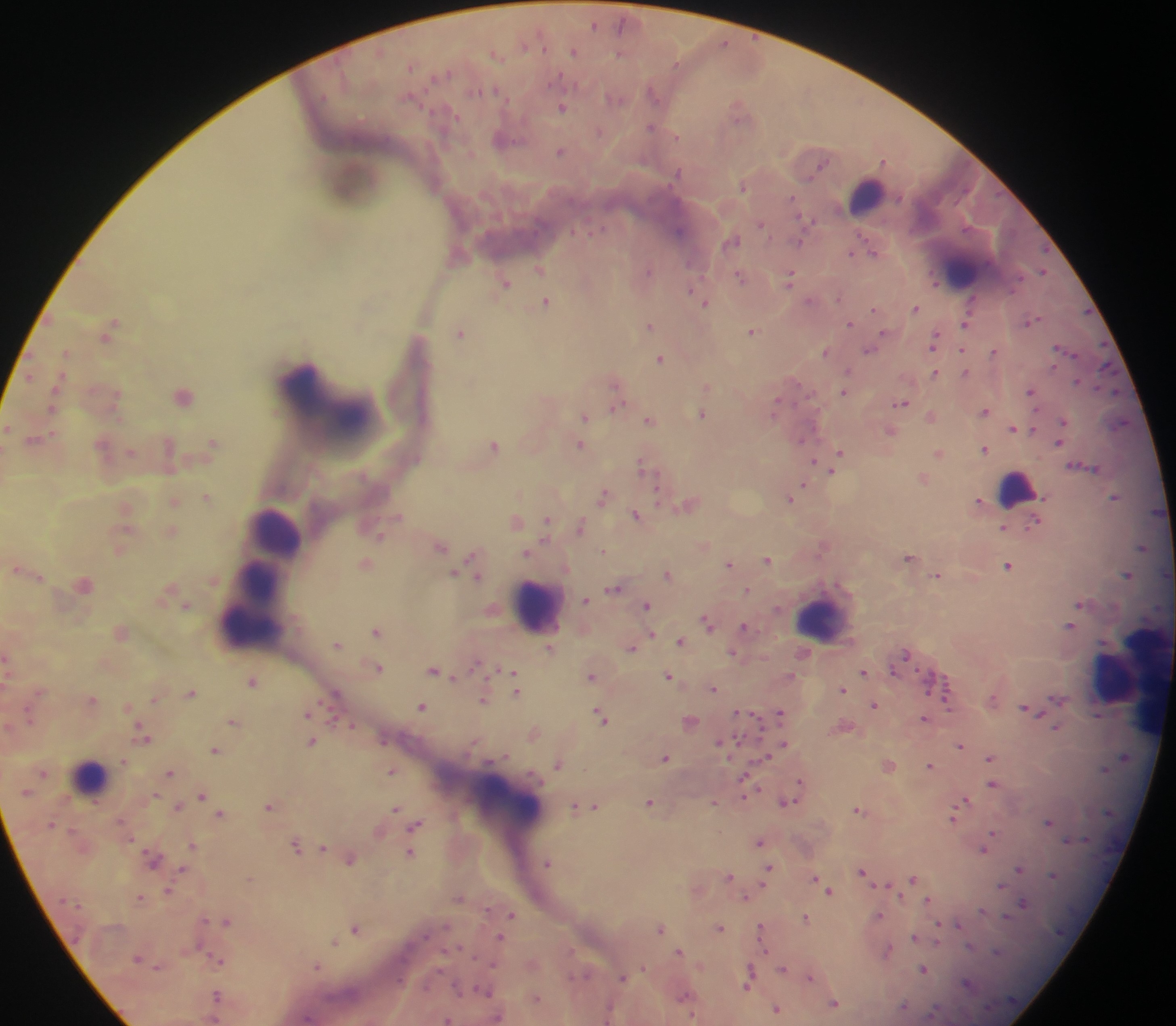
Approximate centers as {x, y} in pixels. Leukocyte locations: {867, 193}, {960, 269}, {1017, 486}, {274, 533}, {262, 592}, {536, 604}, {250, 610}, {823, 616}, {1131, 676}, {1119, 679}, {91, 775}, {507, 803}. Plasmodium parasite locations: {594, 23}, {724, 41}, {574, 49}, {496, 53}, {654, 92}, {615, 97}, {562, 105}, {740, 108}, {653, 125}, {599, 130}, {505, 137}, {560, 150}, {884, 159}, {744, 184}, {761, 222}, {679, 230}, {733, 239}, {799, 240}, {873, 248}, {852, 251}, {458, 254}, {540, 268}, {648, 270}, {1044, 270}, {790, 275}, {741, 276}, {936, 280}, {506, 282}, {973, 299}, {546, 300}, {810, 300}, {705, 301}, {916, 307}, {874, 308}, {850, 322}, {965, 322}, {649, 324}, {752, 329}, {109, 330}, {461, 331}, {886, 333}, {936, 339}, {871, 348}, {961, 348}, {1062, 348}, {826, 350}, {994, 350}, {67, 352}, {661, 357}, {848, 369}, {935, 371}, {966, 371}, {1078, 380}, {616, 383}, {707, 385}, {55, 390}, {1032, 390}, {844, 392}, {184, 394}, {777, 401}, {901, 402}, {616, 405}, {986, 409}, {703, 413}, {931, 415}, {585, 416}, {650, 418}, {1064, 420}, {1121, 422}, {8, 425}, {1013, 426}, {1035, 427}, {892, 429}, {35, 439}, {801, 439}, {1059, 441}, {214, 442}, {494, 444}, {581, 444}, {985, 448}, {131, 451}, {841, 451}, {939, 452}, {816, 460}, {643, 464}, {833, 470}, {924, 477}, {805, 484}, {604, 494}, {206, 495}, {791, 496}, {1116, 496}, {174, 500}, {979, 500}, {690, 503}, {126, 509}, {638, 513}, {517, 519}, {547, 519}, {1036, 520}, {581, 524}, {1005, 526}, {172, 530}, {380, 533}, {441, 543}, {703, 544}, {823, 545}, {1143, 545}, {119, 548}, {605, 550}, {528, 551}, {910, 556}, {767, 558}, {366, 561}, {476, 561}, {730, 563}, {1009, 564}, {19, 569}, {454, 572}, {668, 573}, {1128, 573}, {477, 574}, {40, 575}, {938, 575}, {84, 583}, {615, 586}, {747, 590}, {585, 599}, {1081, 603}, {187, 604}, {647, 605}, {707, 620}, {746, 626}, {1070, 626}, {378, 629}, {121, 630}, {652, 634}, {681, 640}, {338, 643}, {632, 646}, {550, 647}, {734, 652}, {906, 654}, {378, 666}, {435, 669}, {512, 671}, {864, 671}, {592, 674}, {669, 675}, {253, 679}, {714, 688}, {843, 688}, {517, 690}, {191, 692}, {335, 692}, {92, 698}, {155, 698}, {484, 698}, {1058, 698}, {993, 699}, {875, 704}, {127, 706}, {422, 706}, {1026, 709}, {737, 711}, {308, 712}, {780, 712}, {602, 714}, {1099, 715}, {925, 717}, {234, 720}, {690, 720}, {352, 724}, {1057, 727}, {534, 732}, {143, 733}, {312, 740}, {735, 740}, {720, 741}, {784, 743}, {960, 743}, {216, 750}, {666, 756}, {766, 756}, {991, 756}, {1125, 757}, {124, 759}, {559, 762}, {889, 763}, {931, 765}, {992, 768}, {393, 770}, {170, 772}, {802, 781}, {993, 783}, {746, 785}, {202, 794}, {650, 801}, {715, 801}, {788, 801}, {965, 801}, {271, 804}, {593, 804}, {178, 805}, {576, 806}, {959, 807}, {395, 808}, {860, 808}, {220, 813}, {954, 815}, {1049, 822}, {415, 824}, {994, 834}, {760, 841}, {297, 844}, {193, 845}, {324, 846}, {984, 848}, {411, 851}, {153, 857}, {350, 857}, {548, 861}, {1020, 867}, {182, 869}, {769, 869}, {863, 871}, {729, 876}, {816, 877}, {914, 877}, {821, 883}, {1002, 884}, {887, 885}, {169, 890}, {830, 890}, {141, 896}, {459, 897}, {746, 897}, {929, 899}, {1024, 903}, {512, 914}, {878, 915}, {806, 917}, {227, 920}, {958, 924}, {356, 927}, {661, 927}, {720, 927}, {762, 929}, {915, 935}, {501, 937}, {333, 940}, {939, 940}, {681, 950}, {887, 950}, {218, 959}, {318, 965}, {643, 967}, {784, 968}, {924, 969}, {810, 975}, {622, 977}, {750, 977}, {967, 983}, {485, 991}, {218, 994}, {686, 996}, {536, 997}, {834, 1003}, {904, 1007}, {777, 1009}, {447, 1019}. Thick blood smear. Sample from Ghana. Photographed through a microscope with a mobile-phone camera. One field of view. Image is 1176×1026 pixels.